State which cell type is depicted.
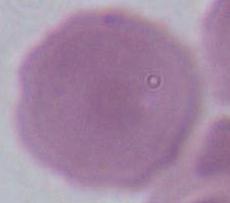
This is an erythrocyte.

Photomicrograph. Captured at 1000x magnification.